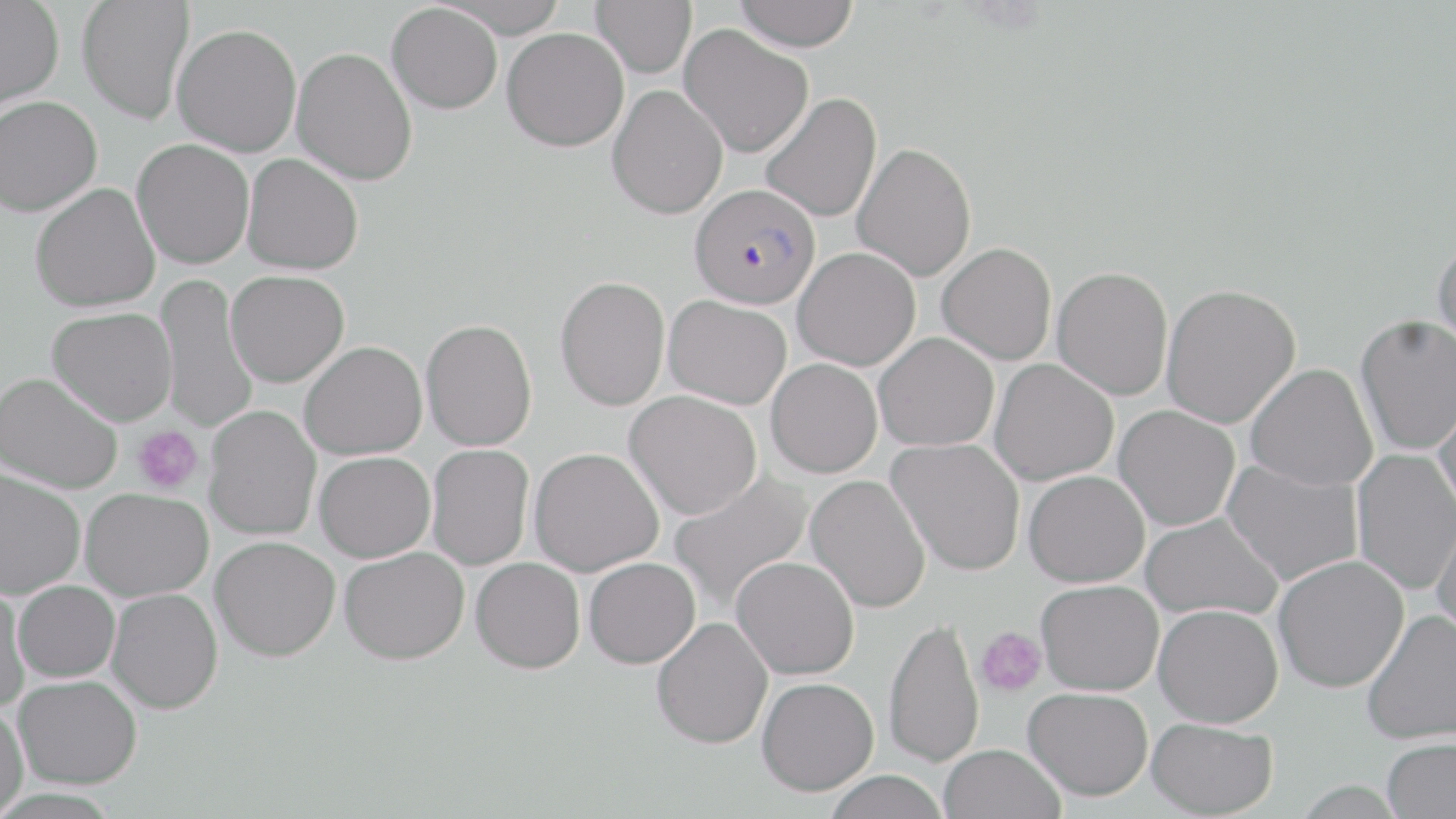

{
  "plasmodium_falciparum_infected_red_blood_cell_locations": "approximate bounding boxes as (x1, y1, x2, y2) in pixels: (690, 183, 820, 309)",
  "slide_level_diagnosis": "Plasmodium falciparum",
  "uninfected_red_blood_cell_locations": "approximate bounding boxes as (x1, y1, x2, y2) in pixels: (77, 0, 195, 124), (432, 0, 571, 38), (591, 0, 696, 78), (733, 0, 859, 52), (0, 1, 64, 109), (386, 3, 502, 114), (172, 23, 302, 156), (679, 24, 814, 158), (502, 27, 629, 152), (291, 47, 418, 185), (606, 85, 728, 219), (760, 92, 882, 223), (0, 95, 102, 216), (132, 138, 254, 269), (852, 142, 977, 282), (242, 153, 364, 274), (31, 182, 160, 312), (1431, 234, 1456, 357), (937, 242, 1057, 365), (793, 247, 921, 371), (1052, 266, 1173, 401), (226, 270, 349, 387), (155, 273, 258, 436), (555, 275, 670, 411), (1161, 283, 1301, 429), (663, 295, 792, 409), (47, 307, 177, 426), (1354, 314, 1456, 456), (420, 318, 537, 451), (874, 332, 999, 452), (299, 341, 427, 460), (766, 358, 882, 478), (989, 358, 1118, 486), (1244, 363, 1378, 492), (0, 372, 123, 494), (624, 391, 762, 520), (1432, 395, 1456, 520), (204, 405, 321, 541), (1114, 405, 1240, 531), (887, 437, 1025, 576), (426, 444, 534, 570), (529, 447, 664, 576), (1350, 448, 1456, 595), (314, 451, 435, 562), (1221, 459, 1363, 587), (0, 467, 86, 598), (1022, 470, 1150, 588), (669, 472, 813, 615), (806, 475, 931, 613), (80, 488, 213, 601), (1141, 512, 1283, 622), (1431, 512, 1456, 645), (211, 536, 340, 661), (339, 546, 469, 664), (731, 555, 859, 680), (1273, 555, 1408, 692), (471, 557, 585, 673), (584, 557, 701, 669), (1036, 580, 1164, 695), (13, 581, 120, 682), (0, 582, 32, 712), (107, 588, 223, 714), (1153, 604, 1283, 727), (1361, 610, 1456, 745), (652, 617, 773, 749), (883, 617, 984, 767), (14, 674, 142, 788), (756, 677, 878, 796), (1023, 687, 1153, 800), (0, 701, 28, 819), (1146, 716, 1278, 818), (1381, 737, 1456, 819), (939, 744, 1065, 819), (823, 770, 949, 819)",
  "platelet_locations": "approximate bounding boxes as (x1, y1, x2, y2) in pixels: (133, 425, 203, 494), (975, 627, 1046, 698)",
  "preparation": "thin blood smear",
  "stain": "May-Grünwald-Giemsa",
  "image_size": "1456×819 pixels",
  "modality": "light microscopy",
  "magnification": "1000x",
  "field_of_view": "one of a larger specimen"
}